Report the malaria status of this cell.
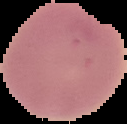
Uninfected.

Segmented cell region on a black background. From a thin blood smear. Image is 127×124 pixels.